Locate every uninfected red blood cell.
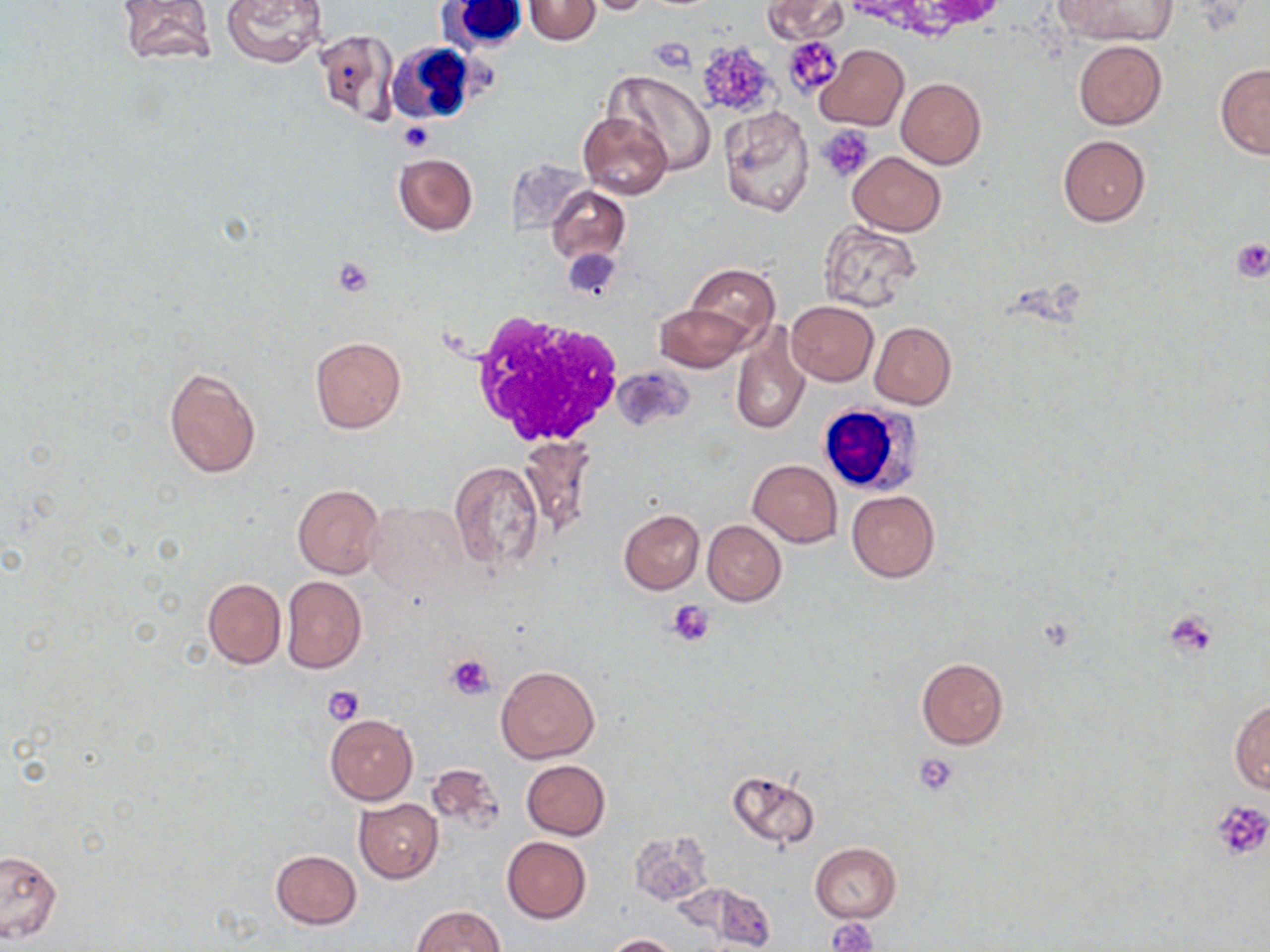
Approximate bounding boxes as (x1,y1)-(x2,y2) corner pairs in pixels.
Uninfected red blood cells (subset): (115,0)-(217,64), (220,0)-(327,66), (524,0)-(600,45), (581,0)-(662,16), (764,0)-(847,43), (1055,0)-(1176,46), (313,28)-(399,127), (1074,40)-(1166,129), (815,44)-(908,131), (1215,64)-(1270,159), (607,69)-(717,175), (896,78)-(986,168), (719,107)-(814,218), (577,112)-(673,200), (1057,135)-(1151,226), (846,152)-(946,236), (393,153)-(478,236), (546,185)-(629,264), (818,222)-(921,312), (688,264)-(780,345), (785,301)-(878,385), (655,303)-(751,373), (869,321)-(956,409), (730,324)-(810,439), (310,337)-(406,433), (162,366)-(261,479), (517,437)-(597,541), (749,460)-(843,546), (450,462)-(544,575), (292,484)-(384,579), (847,490)-(940,582), (364,500)-(467,596), (619,509)-(704,594), (703,520)-(785,606), (281,575)-(367,674), (202,578)-(286,669), (916,658)-(1008,749), (495,665)-(600,763), (1230,697)-(1269,796), (325,713)-(417,804), (520,759)-(611,840), (424,762)-(505,833), (729,770)-(820,851), (353,799)-(443,883), (627,831)-(714,907), (501,836)-(591,923), (810,843)-(901,923), (0,850)-(62,943), (271,850)-(361,929), (684,885)-(775,948), (412,904)-(504,952), (604,934)-(679,952).

Summary:
  - Platelet locations (subset): (784,36)-(842,98), (651,38)-(694,72), (695,41)-(778,120), (399,122)-(432,152), (819,125)-(873,181), (1233,238)-(1270,283), (566,249)-(620,301), (332,258)-(373,297), (668,600)-(716,645), (1167,610)-(1218,657), (448,654)-(497,699), (323,684)-(365,725), (914,751)-(962,795), (1210,800)-(1270,861), (829,918)-(878,952)
  - White blood cell locations: (443,0)-(528,51), (387,41)-(475,123), (467,310)-(623,449), (816,400)-(923,498)
  - Slide-level diagnosis: no evidence of blood parasites
  - Preparation: thin blood smear
  - Modality: light microscopy
  - Image size: 1270×952 pixels
  - Stain: May-Grünwald-Giemsa
  - Field of view: one of a larger specimen
  - Magnification: 1000x